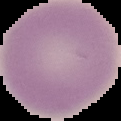

{
  "result": "no malaria parasites detected",
  "image_type": "cell region segmented out of the field of view; surrounding area masked to black",
  "preparation": "thin blood film",
  "image_size": "121×121 pixels"
}